Evaluate for malaria.
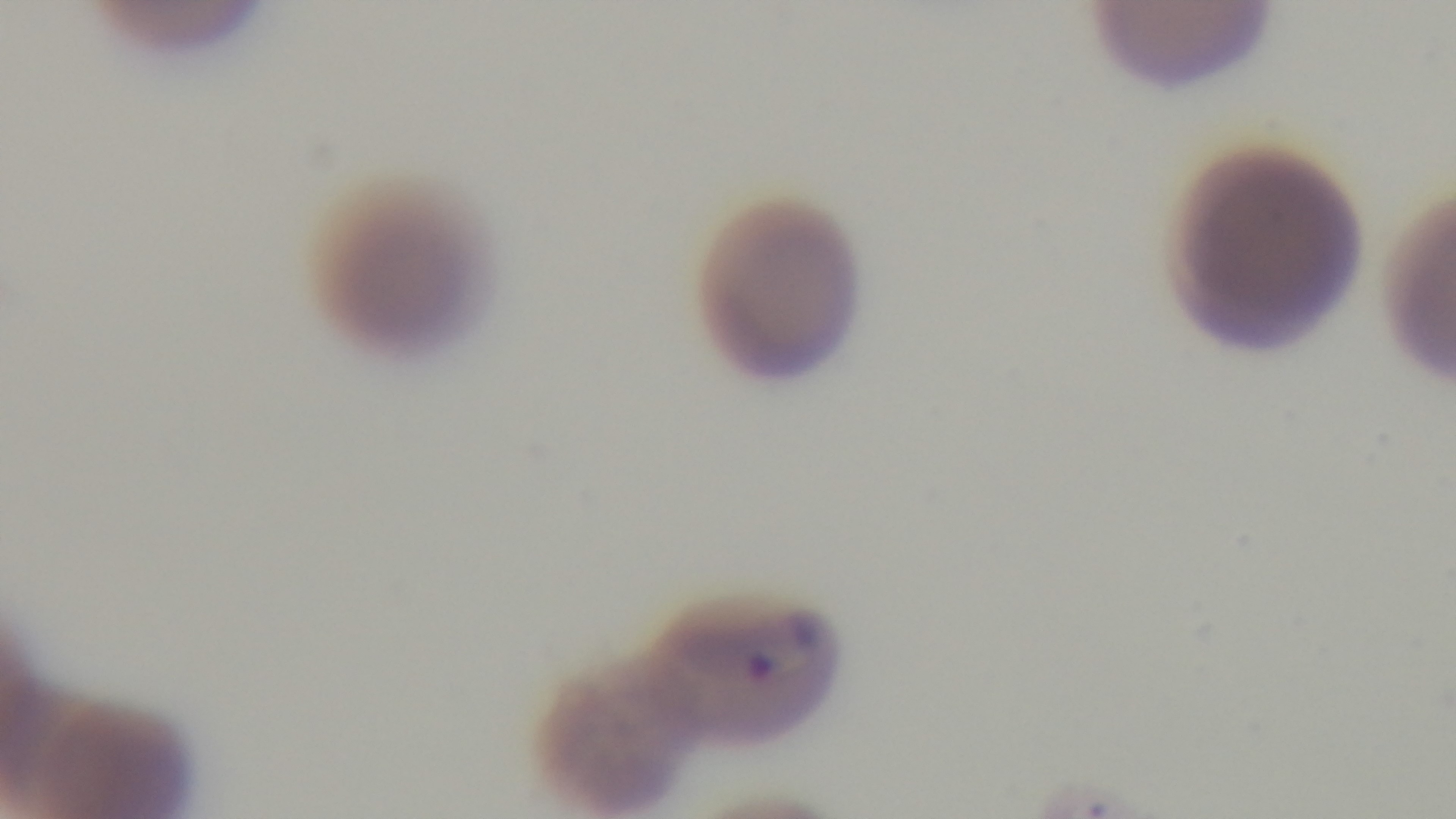
Infected.

One field from the slide. Captured with a mounted 4K digital camera. Preparation: thin. Light microscopy. 100x oil-immersion objective. Giemsa-stained.